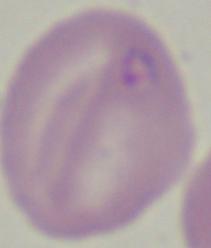
Summary:
  - Magnification: 1000x
  - Identification: Babesia
  - Modality: photomicrograph